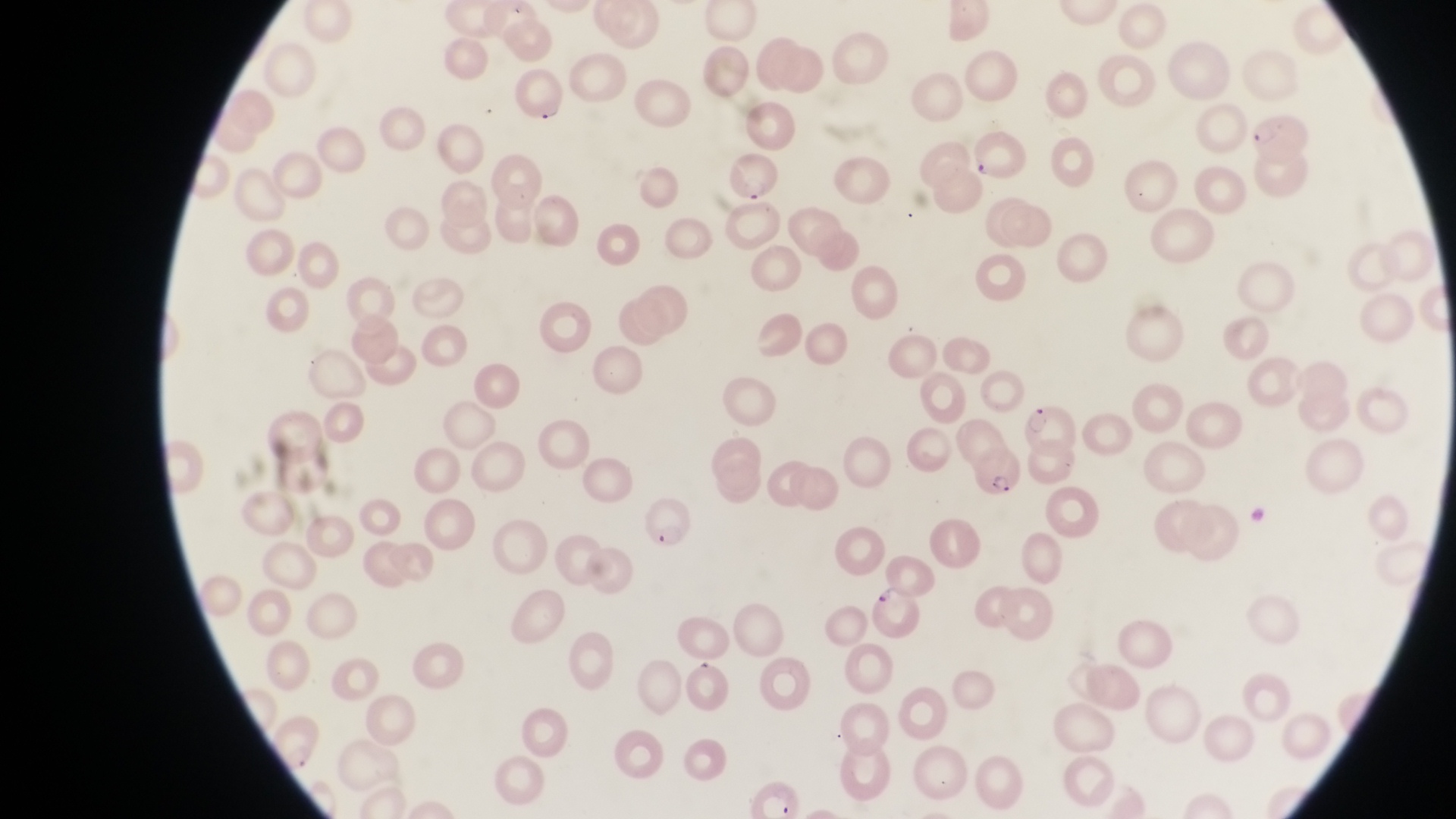
Approximate bounding boxes as {left, top, right, bottom} in pixels.
Summary:
  - Parasitised red blood cell locations: {508, 73, 564, 131}, {1245, 112, 1306, 164}, {724, 155, 776, 204}, {1023, 399, 1075, 452}, {970, 446, 1020, 499}, {641, 497, 694, 547}, {871, 584, 921, 637}
  - Image size: 1456×819 pixels
  - Magnification: 1000x
  - Field of view: single
  - Capture: smartphone photograph through the eyepiece of an Olympus CX-23 microscope
  - Preparation: thin blood smear
  - Country: Uganda